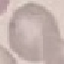
malaria_status: uninfected
stain: Giemsa
capture: smartphone through the microscope eyepiece
image_type: automatically extracted cell patch, resized to 64 × 64 pixels
preparation: thin blood smear